Comment on the morphology of the red blood cells.
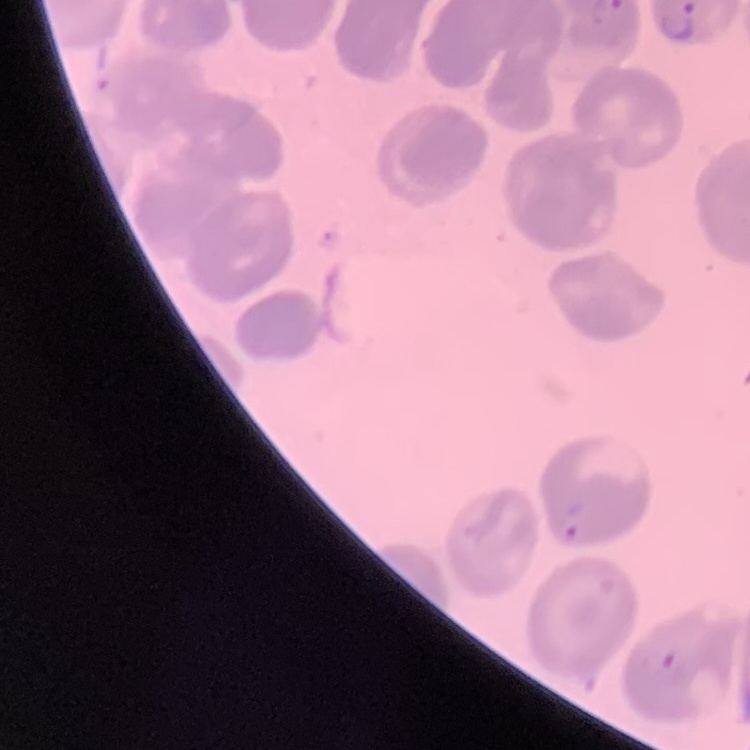

They show no rouleaux formation.

Summary:
  - Image type: square crop of a larger photomicrograph
  - Stain: Field's or Giemsa
  - Preparation: thin blood smear